Identify the preparation type.
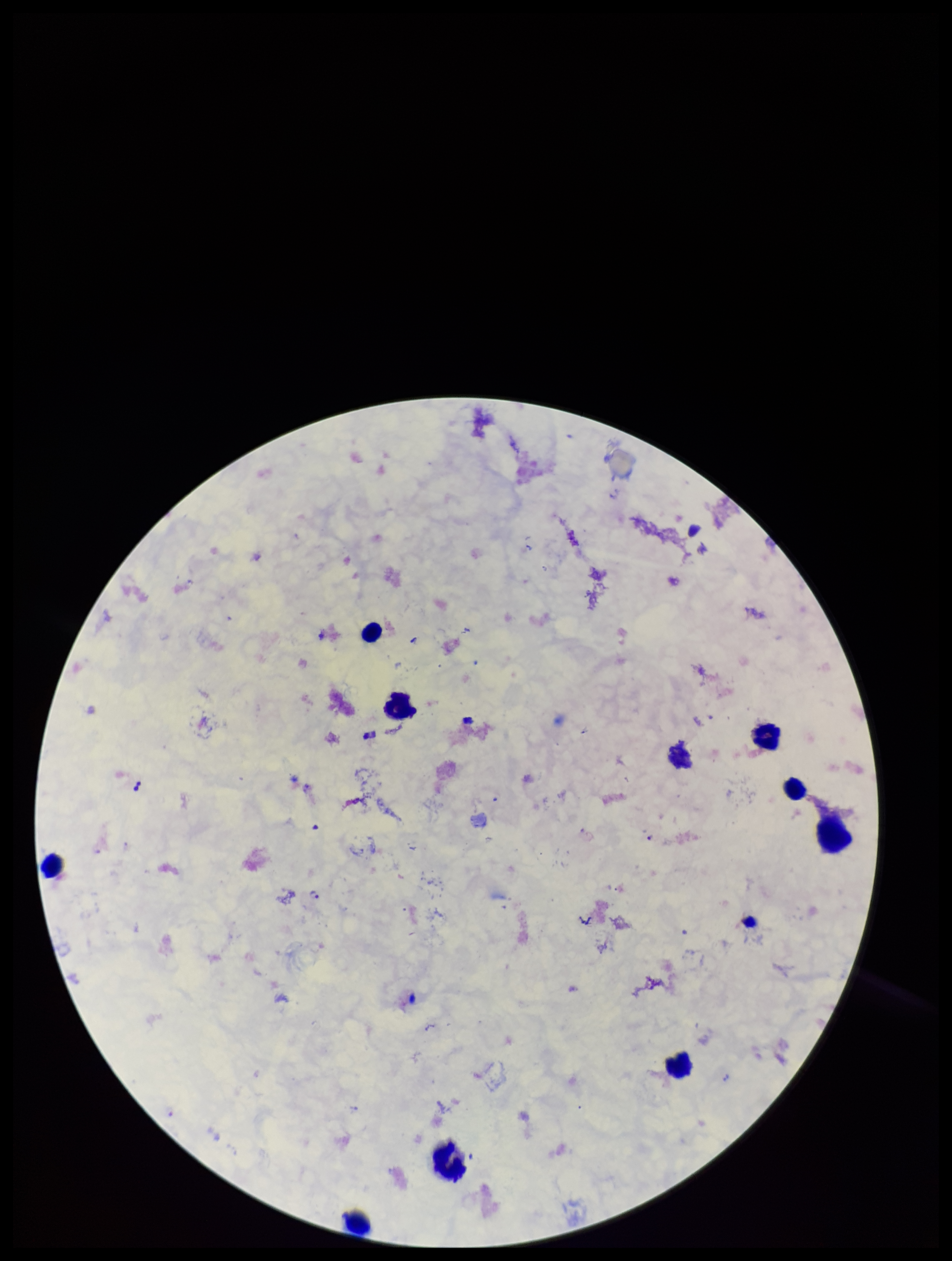
It is a thick blood smear.

{
  "leukocyte_count": 9,
  "species_reported_for_this_patient": "Plasmodium falciparum",
  "parasite_count": 2,
  "field_of_view": "one from this slide",
  "stain": "Giemsa",
  "image_size": "952×1261 pixels",
  "plasmodium_parasites": "detected",
  "capture": "smartphone photograph through the microscope eyepiece",
  "patient_malaria_status": "positive"
}